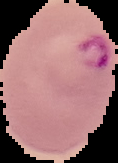

result = Plasmodium parasites detected
image size = 118×163 pixels
preparation = thin blood film
image type = cell region segmented out of the field of view; surrounding area masked to black